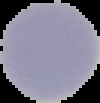

Summary:
  - Result: no Plasmodium parasites seen
  - Image size: 100×103 pixels
  - Preparation: thin blood smear
  - Image type: cell region segmented out of the field of view; surrounding area masked to black